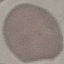

Malaria status: uninfected. Giemsa-stained preparation. Thin blood film. Automatically extracted cell patch, resized to 64 × 64 pixels. Photographed with a smartphone camera at the microscope eyepiece.